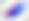

{
  "identification": "Toxoplasma gondii",
  "magnification": "400x",
  "modality": "photomicrograph"
}